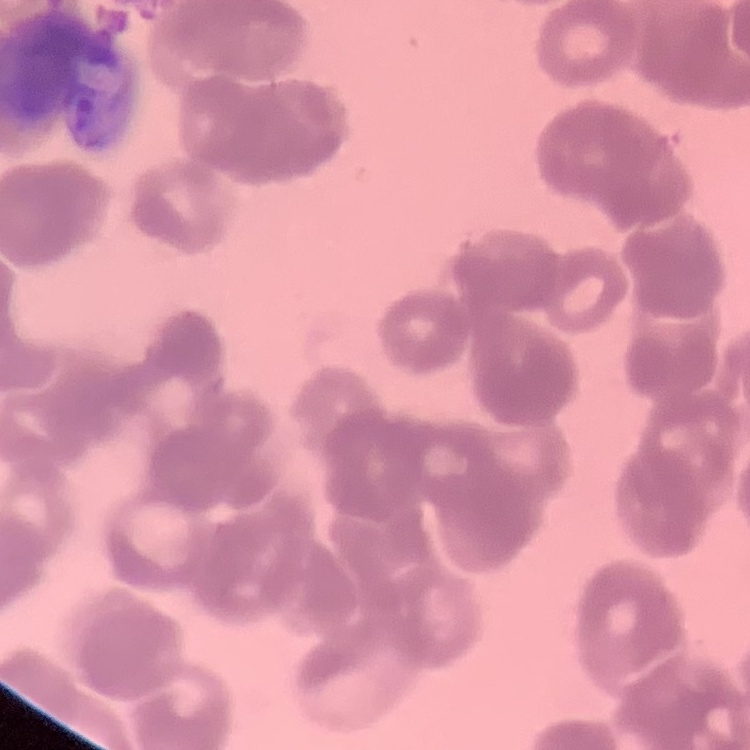

The erythrocytes exhibit rouleaux formation. Thin blood smear. Field's or Giemsa stain. Square crop of a larger photomicrograph.